Outline each Plasmodium malariae-infected red blood cell.
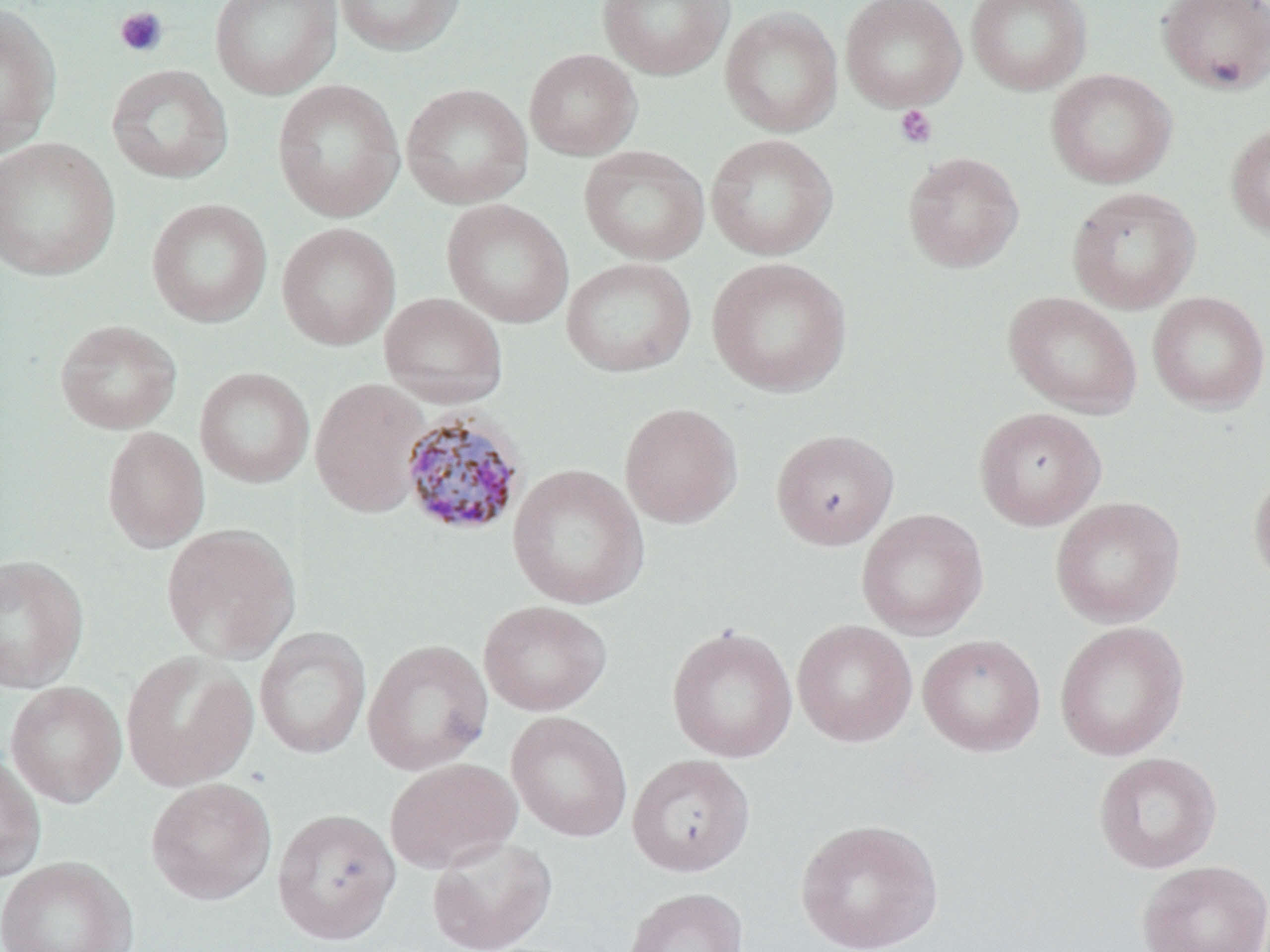

Approximate bounding boxes as [x1, y1, x2, y2] in pixels.
Plasmodium malariae-infected red blood cells: [399, 409, 529, 538].

Platelet locations: [114, 6, 169, 58], [894, 105, 937, 149]. Uninfected red blood cell locations: [209, 0, 342, 100], [334, 0, 467, 57], [596, 0, 734, 80], [841, 0, 966, 112], [966, 0, 1092, 95], [1156, 0, 1270, 94], [0, 2, 62, 158], [719, 7, 843, 138], [524, 49, 642, 160], [106, 64, 234, 184], [1046, 69, 1176, 188], [272, 79, 405, 222], [400, 82, 533, 209], [1225, 121, 1270, 239], [705, 133, 838, 260], [0, 137, 120, 281], [579, 145, 710, 266], [903, 152, 1024, 273], [1067, 187, 1200, 314], [146, 198, 273, 328], [442, 199, 573, 328], [276, 222, 400, 350], [561, 257, 696, 377], [706, 257, 852, 397], [1002, 291, 1143, 418], [1147, 291, 1269, 413], [379, 292, 508, 408], [54, 320, 182, 434], [195, 367, 314, 488], [309, 377, 430, 517], [619, 402, 743, 528], [974, 407, 1106, 530], [101, 426, 209, 553], [771, 429, 899, 550], [507, 464, 649, 610], [1248, 467, 1270, 587], [1049, 496, 1185, 627], [856, 508, 988, 639], [160, 523, 301, 663], [0, 554, 89, 694], [478, 601, 612, 716], [791, 620, 918, 747], [1054, 621, 1189, 761], [666, 624, 799, 763], [254, 626, 371, 760], [917, 634, 1046, 756], [362, 639, 493, 775], [121, 651, 258, 791], [5, 681, 127, 808], [506, 711, 633, 842], [1093, 751, 1222, 874], [0, 752, 47, 883], [626, 754, 755, 876], [384, 757, 521, 874], [146, 778, 277, 906], [272, 807, 401, 944], [795, 817, 944, 952], [427, 835, 557, 951], [0, 856, 138, 952], [1137, 859, 1269, 952], [623, 887, 748, 952]. Slide-level diagnosis: Plasmodium malariae. Light microscopy. May-Grünwald-Giemsa stain. Thin blood film. Captured at 1000x magnification. Image is 1270×952 pixels. Single field of view.